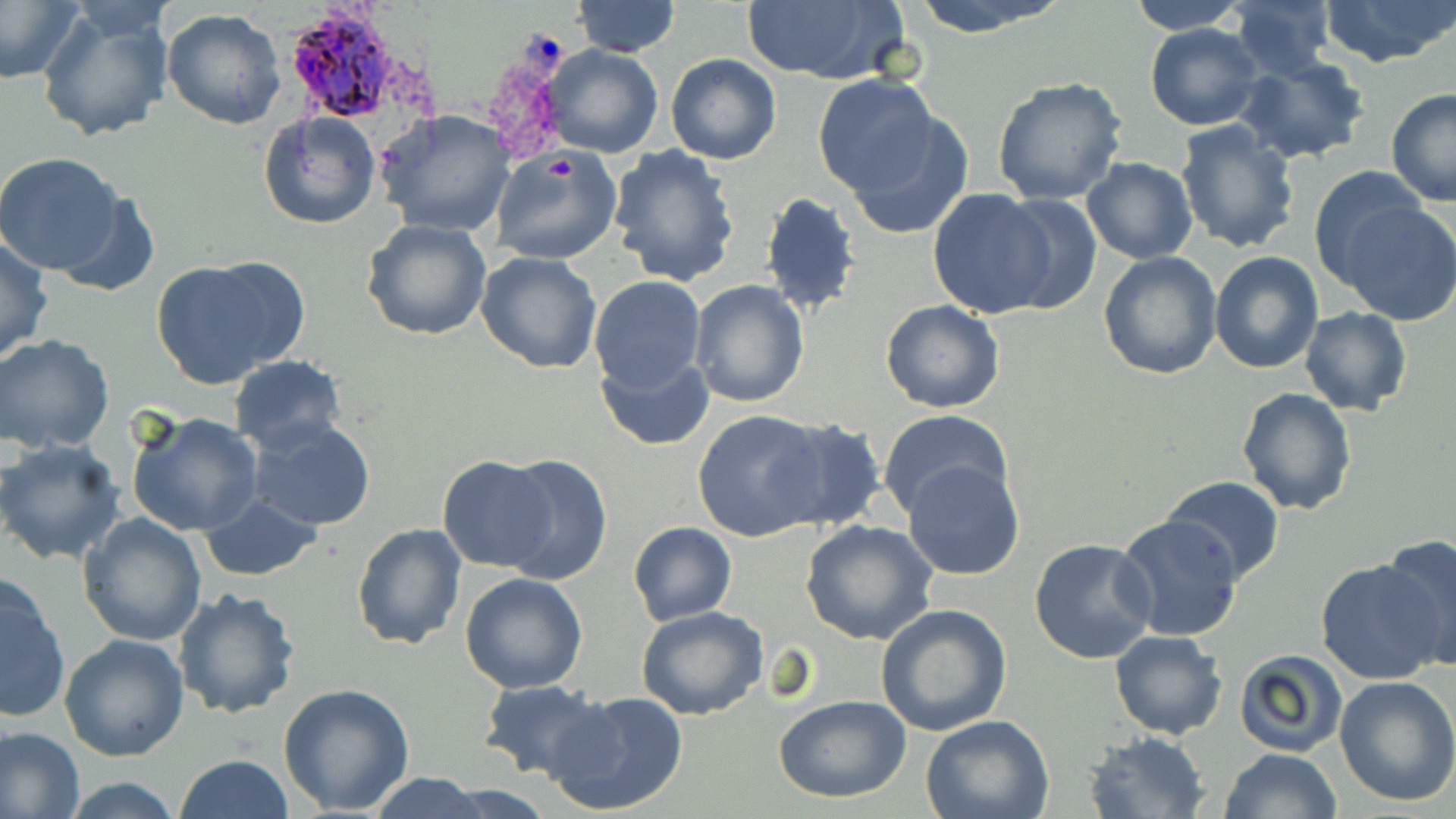
slide-level diagnosis = Plasmodium ovale
stain = May-Grünwald-Giemsa
image size = 1456×819 pixels
modality = light microscopy
magnification = 1000x
field of view = single
preparation = thin blood film
Plasmodium ovale-infected red blood cell locations = approximate bounding boxes as [x1, y1, x2, y2] in pixels: [284, 3, 416, 124]
uninfected red blood cell locations = approximate bounding boxes as [x1, y1, x2, y2] in pixels: [0, 0, 84, 85], [571, 0, 679, 57], [904, 0, 1071, 37], [1123, 0, 1253, 34], [1226, 0, 1336, 79], [1321, 0, 1455, 68], [740, 1, 910, 85], [34, 4, 176, 144], [161, 9, 285, 130], [1144, 23, 1263, 131], [543, 46, 664, 159], [666, 53, 780, 165], [1235, 57, 1370, 164], [990, 76, 1130, 208], [815, 77, 957, 219], [1386, 89, 1456, 206], [376, 109, 516, 239], [257, 110, 382, 228], [1173, 118, 1301, 253], [490, 145, 622, 264], [607, 145, 741, 288], [0, 152, 129, 277], [1081, 158, 1197, 264], [1308, 165, 1428, 287], [928, 189, 1058, 320], [51, 191, 160, 299], [761, 192, 861, 314], [995, 194, 1102, 314], [1338, 200, 1456, 327], [361, 219, 492, 340], [0, 235, 53, 363], [476, 250, 601, 373], [1098, 251, 1222, 378], [1210, 251, 1323, 373], [149, 258, 298, 389], [589, 275, 706, 393], [689, 279, 811, 408], [880, 300, 1005, 414], [1299, 308, 1414, 415], [0, 332, 115, 454], [593, 352, 713, 451], [228, 355, 347, 455], [1236, 386, 1358, 516], [876, 409, 1014, 521], [692, 410, 829, 543], [126, 411, 263, 536], [768, 417, 887, 532], [245, 418, 377, 532], [0, 439, 127, 567], [498, 453, 612, 586], [437, 455, 555, 572], [903, 458, 1024, 580], [1160, 474, 1285, 583], [199, 496, 322, 581], [77, 512, 206, 646], [1114, 514, 1243, 643], [628, 521, 737, 625], [800, 521, 938, 646], [351, 522, 467, 650], [1380, 534, 1456, 669], [1029, 537, 1160, 666], [1315, 559, 1447, 687], [459, 571, 589, 694], [1, 575, 70, 724], [173, 587, 301, 720], [874, 603, 1011, 738], [636, 605, 768, 720], [1109, 632, 1228, 739], [59, 633, 189, 759], [1233, 648, 1347, 758], [1334, 675, 1456, 808], [477, 680, 608, 782], [277, 682, 415, 815], [548, 690, 690, 818], [774, 695, 913, 803], [921, 713, 1055, 819], [0, 724, 85, 819], [1081, 731, 1211, 818], [1220, 748, 1344, 819], [174, 753, 292, 819], [364, 773, 492, 818], [60, 776, 187, 817]